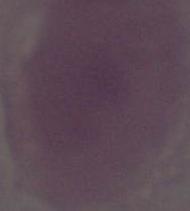

Summary:
  - Modality: photomicrograph
  - Identification: erythrocyte
  - Magnification: 1000x